Assess the morphology of the red blood cells.
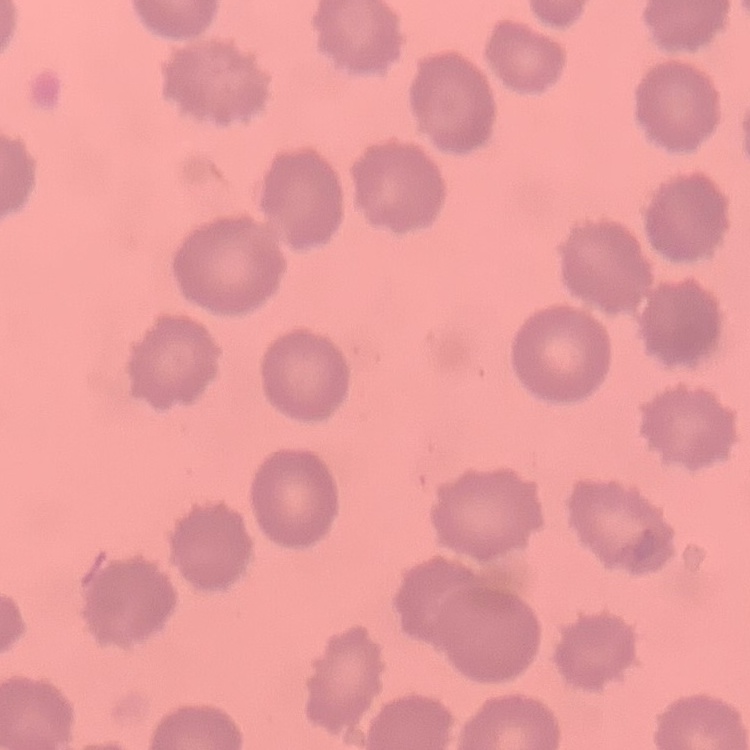
No rouleaux formation.

One tile cut from a larger photomicrograph. Stained with either Field's or Giemsa. Thin blood smear.